Comment on the morphology of the erythrocytes.
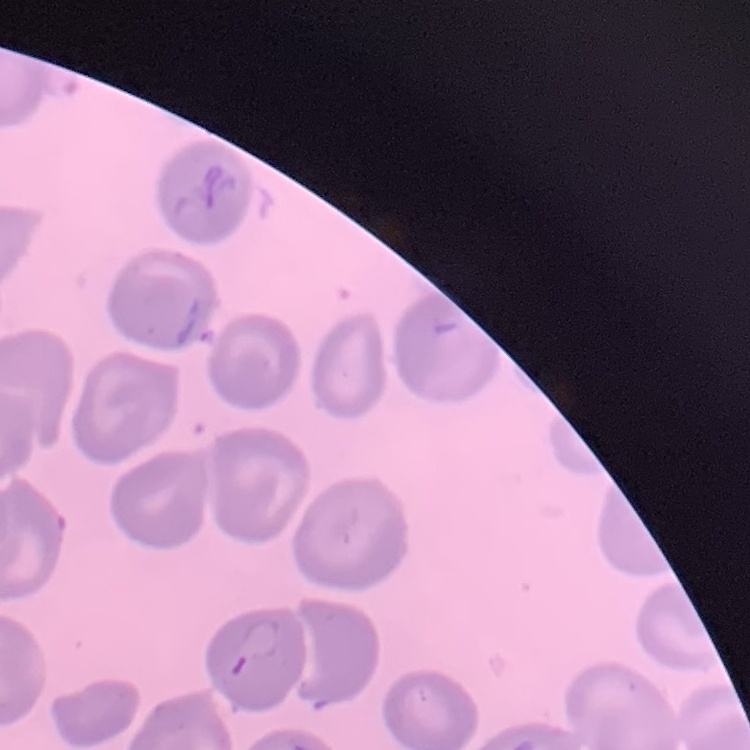
They show no rouleaux formation.

Stained with either Field's or Giemsa. Thin blood film. Square crop of a larger photomicrograph.